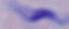

Summary:
  - Modality: micrograph
  - Magnification: 1000x
  - Identification: trypanosome